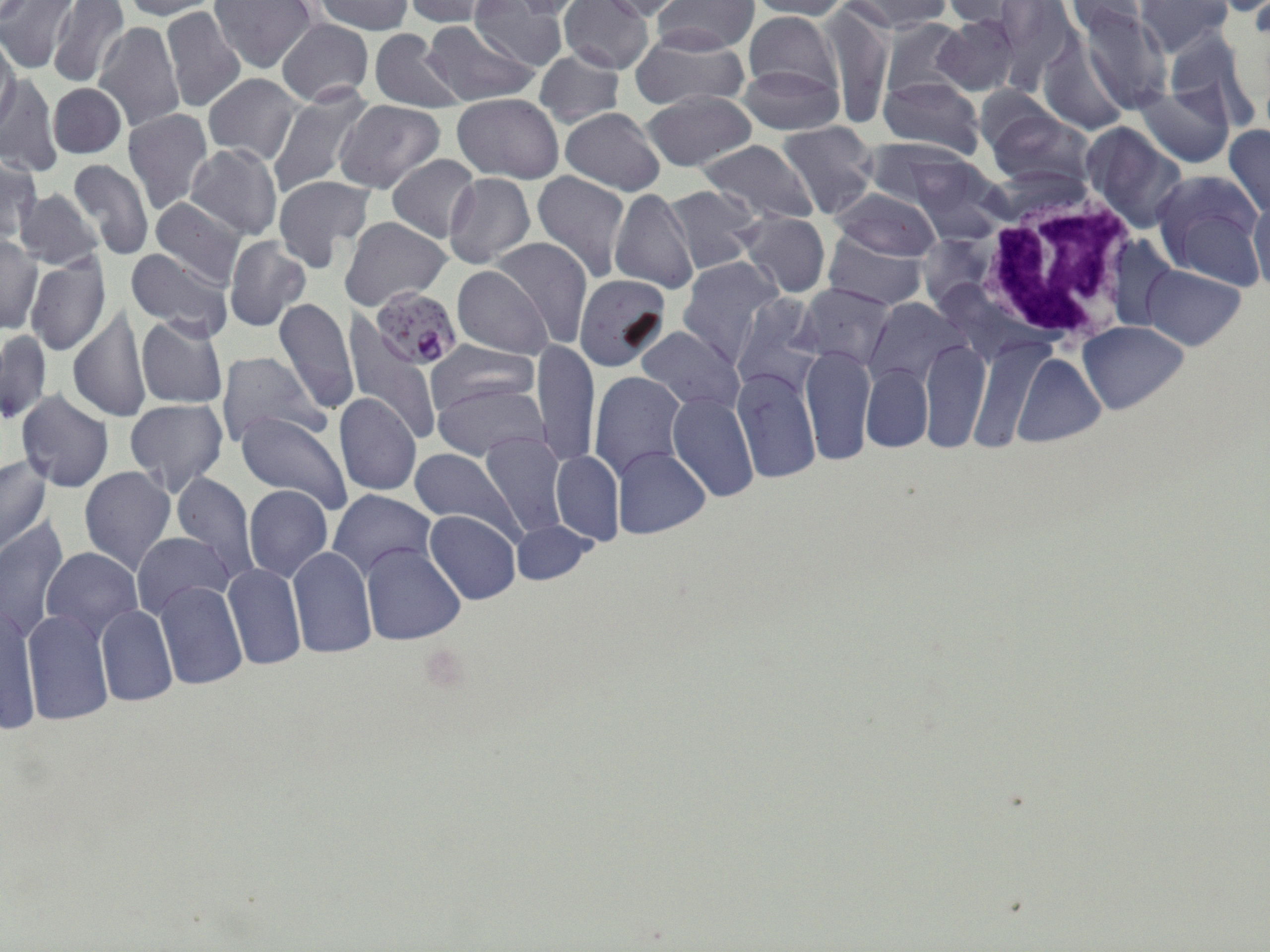
{
  "slide_level_diagnosis": "Plasmodium falciparum",
  "magnification": "1000x",
  "modality": "optical microscopy",
  "plasmodium_falciparum_infected_red_blood_cell_locations": "approximate bounding boxes as named x1/y1/x2/y2 corners in pixels: (x1=373, y1=290, x2=466, y2=372)",
  "preparation": "thin blood film",
  "stain": "May-Grünwald-Giemsa",
  "image_size": "1270×952 pixels",
  "uninfected_red_blood_cell_locations": "approximate bounding boxes as named x1/y1/x2/y2 corners in pixels: (x1=0, y1=0, x2=77, y2=73), (x1=46, y1=0, x2=131, y2=90), (x1=119, y1=0, x2=220, y2=20), (x1=209, y1=0, x2=316, y2=73), (x1=310, y1=0, x2=414, y2=36), (x1=401, y1=0, x2=500, y2=27), (x1=497, y1=0, x2=584, y2=21), (x1=559, y1=0, x2=655, y2=74), (x1=596, y1=0, x2=692, y2=21), (x1=746, y1=0, x2=854, y2=19), (x1=842, y1=0, x2=949, y2=33), (x1=938, y1=0, x2=1032, y2=27), (x1=1063, y1=0, x2=1161, y2=38), (x1=470, y1=1, x2=571, y2=70), (x1=654, y1=1, x2=757, y2=54), (x1=1135, y1=1, x2=1232, y2=54), (x1=160, y1=6, x2=246, y2=113), (x1=823, y1=7, x2=892, y2=129), (x1=1075, y1=9, x2=1172, y2=112), (x1=743, y1=11, x2=842, y2=105), (x1=933, y1=15, x2=1020, y2=96), (x1=275, y1=18, x2=374, y2=106), (x1=418, y1=19, x2=540, y2=108), (x1=880, y1=19, x2=967, y2=99), (x1=93, y1=21, x2=185, y2=132), (x1=368, y1=28, x2=465, y2=113), (x1=630, y1=31, x2=748, y2=112), (x1=0, y1=35, x2=19, y2=128), (x1=1039, y1=40, x2=1130, y2=134), (x1=535, y1=50, x2=624, y2=127), (x1=738, y1=63, x2=841, y2=135), (x1=202, y1=73, x2=301, y2=167), (x1=1, y1=75, x2=60, y2=175), (x1=879, y1=75, x2=985, y2=160), (x1=265, y1=83, x2=374, y2=200), (x1=1137, y1=83, x2=1234, y2=166), (x1=48, y1=84, x2=125, y2=159), (x1=641, y1=90, x2=756, y2=171), (x1=451, y1=93, x2=564, y2=184), (x1=335, y1=99, x2=444, y2=193), (x1=558, y1=107, x2=665, y2=195), (x1=123, y1=108, x2=213, y2=213), (x1=985, y1=109, x2=1093, y2=190), (x1=774, y1=121, x2=879, y2=218), (x1=1080, y1=125, x2=1186, y2=232), (x1=1224, y1=125, x2=1270, y2=217), (x1=697, y1=139, x2=817, y2=227), (x1=185, y1=143, x2=282, y2=240), (x1=386, y1=154, x2=480, y2=241), (x1=904, y1=156, x2=1006, y2=241), (x1=0, y1=157, x2=41, y2=243), (x1=65, y1=158, x2=151, y2=262), (x1=1152, y1=171, x2=1263, y2=285), (x1=532, y1=172, x2=630, y2=281), (x1=443, y1=173, x2=535, y2=268), (x1=272, y1=175, x2=374, y2=272), (x1=665, y1=185, x2=761, y2=276), (x1=14, y1=187, x2=103, y2=269), (x1=610, y1=188, x2=699, y2=294), (x1=831, y1=189, x2=941, y2=261), (x1=149, y1=196, x2=248, y2=289), (x1=1248, y1=196, x2=1270, y2=292), (x1=736, y1=212, x2=830, y2=296), (x1=340, y1=217, x2=450, y2=312), (x1=824, y1=231, x2=927, y2=309), (x1=0, y1=234, x2=41, y2=334), (x1=224, y1=237, x2=311, y2=331), (x1=489, y1=237, x2=592, y2=347), (x1=125, y1=249, x2=235, y2=342), (x1=24, y1=252, x2=111, y2=354), (x1=678, y1=257, x2=784, y2=369), (x1=1144, y1=264, x2=1244, y2=350), (x1=453, y1=265, x2=553, y2=360), (x1=574, y1=275, x2=671, y2=372), (x1=797, y1=283, x2=894, y2=371), (x1=273, y1=298, x2=359, y2=414), (x1=863, y1=298, x2=966, y2=390), (x1=68, y1=307, x2=150, y2=423), (x1=136, y1=315, x2=227, y2=409), (x1=1079, y1=323, x2=1188, y2=413), (x1=343, y1=324, x2=438, y2=446), (x1=637, y1=326, x2=740, y2=413), (x1=1, y1=327, x2=51, y2=424), (x1=920, y1=339, x2=990, y2=450), (x1=534, y1=340, x2=600, y2=467), (x1=426, y1=341, x2=540, y2=416), (x1=801, y1=345, x2=874, y2=465), (x1=968, y1=345, x2=1040, y2=450), (x1=217, y1=351, x2=325, y2=449), (x1=1014, y1=353, x2=1104, y2=446), (x1=862, y1=364, x2=933, y2=453), (x1=733, y1=368, x2=820, y2=483), (x1=588, y1=371, x2=685, y2=481), (x1=607, y1=376, x2=741, y2=494), (x1=431, y1=379, x2=548, y2=461), (x1=16, y1=390, x2=114, y2=492), (x1=666, y1=393, x2=758, y2=502), (x1=334, y1=394, x2=421, y2=497), (x1=125, y1=399, x2=227, y2=494), (x1=236, y1=412, x2=352, y2=513), (x1=477, y1=431, x2=570, y2=539), (x1=409, y1=447, x2=518, y2=537), (x1=613, y1=447, x2=711, y2=539), (x1=550, y1=450, x2=623, y2=545), (x1=0, y1=457, x2=53, y2=556), (x1=80, y1=467, x2=176, y2=574), (x1=171, y1=472, x2=259, y2=583), (x1=244, y1=485, x2=333, y2=582), (x1=329, y1=488, x2=435, y2=580), (x1=425, y1=511, x2=520, y2=605), (x1=0, y1=519, x2=69, y2=642), (x1=513, y1=522, x2=592, y2=585), (x1=246, y1=528, x2=354, y2=631), (x1=131, y1=530, x2=233, y2=621), (x1=360, y1=544, x2=466, y2=645), (x1=42, y1=547, x2=141, y2=638), (x1=288, y1=547, x2=376, y2=658), (x1=222, y1=564, x2=306, y2=669), (x1=154, y1=581, x2=247, y2=691), (x1=1, y1=601, x2=39, y2=735), (x1=97, y1=605, x2=177, y2=706), (x1=22, y1=608, x2=114, y2=725)",
  "field_of_view": "one of a larger specimen",
  "white_blood_cell_locations": "approximate bounding boxes as named x1/y1/x2/y2 corners in pixels: (x1=1079, y1=124, x2=1189, y2=233), (x1=973, y1=176, x2=1143, y2=350)"
}